Assess the morphology of the red blood cells.
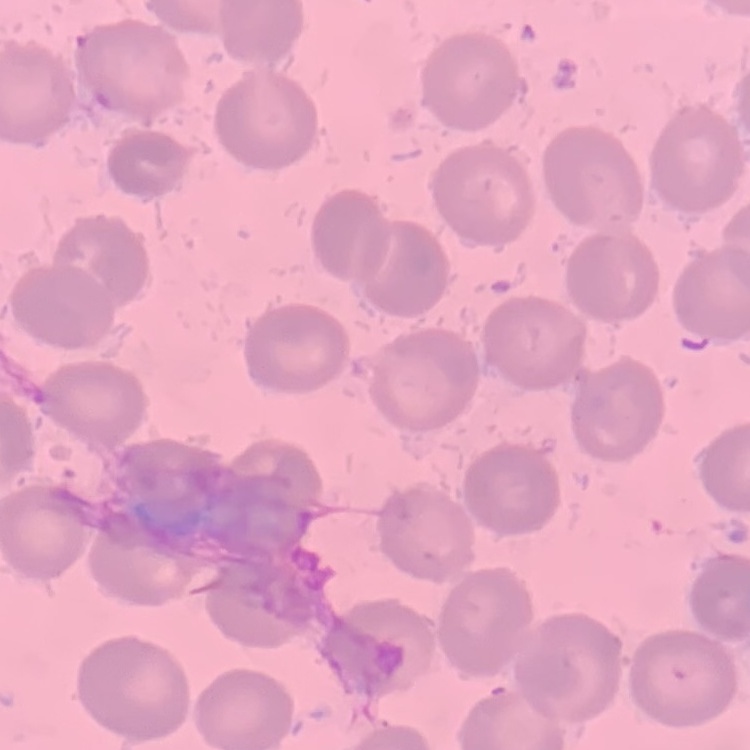

They show no rouleaux formation.

image type = square crop of a larger photomicrograph
stain = Field's or Giemsa
preparation = thin blood film